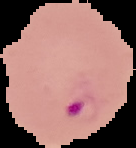
preparation = thin blood smear
image type = segmented cell region on a black background
image size = 136×148 pixels
malaria status = parasitized